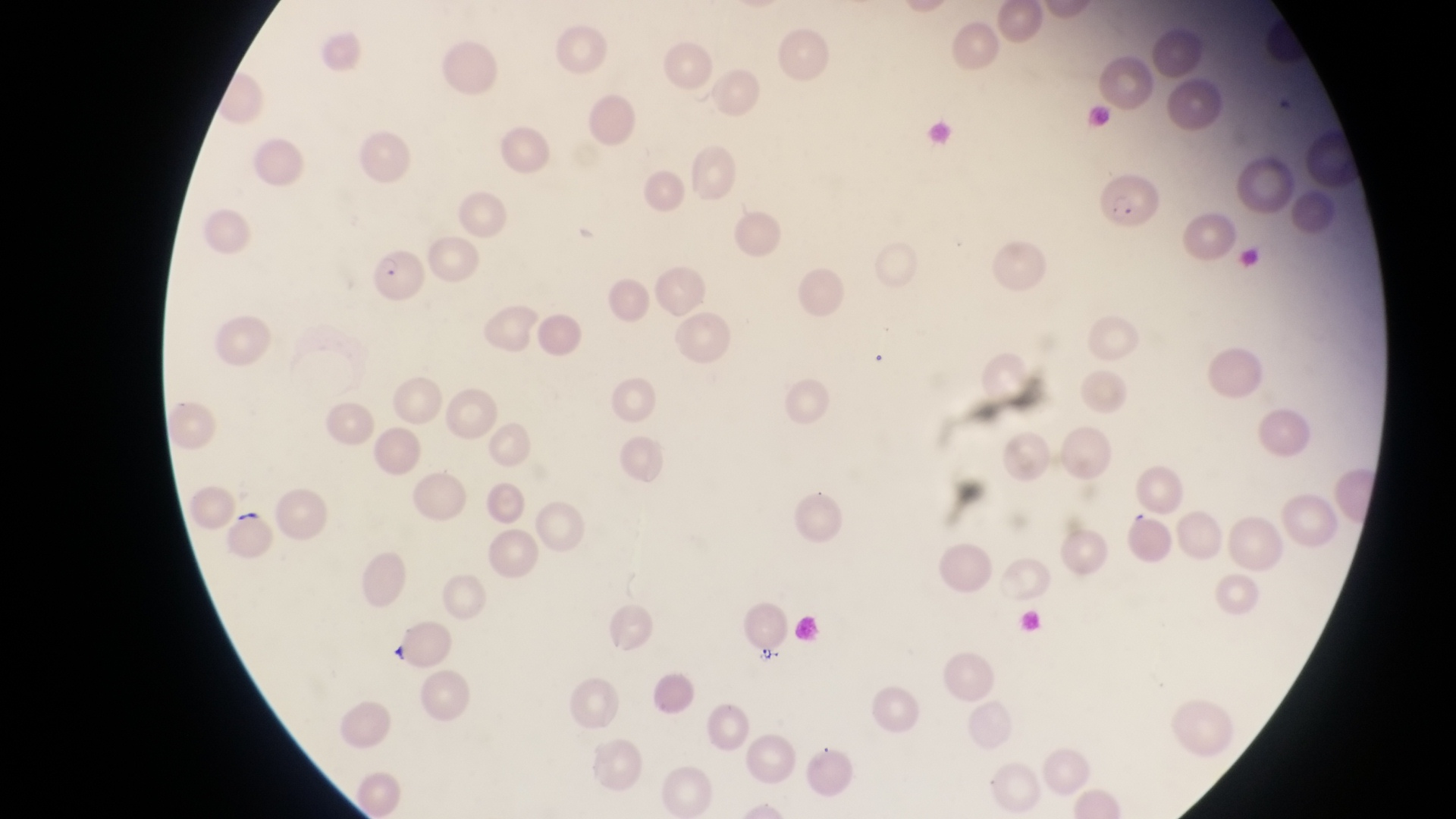
trophozoite locations = approximate bounding boxes as {left, top, right, bottom} in pixels: {755, 644, 781, 667}
country = Uganda
image size = 1456×819 pixels
parasitised red blood cell locations = approximate bounding boxes as {left, top, right, bottom} in pixels: {1097, 171, 1163, 230}, {367, 248, 425, 307}
capture = smartphone photograph through the eyepiece of an Olympus CX-23 microscope
preparation = thin blood film
field of view = single
magnification = 1000x